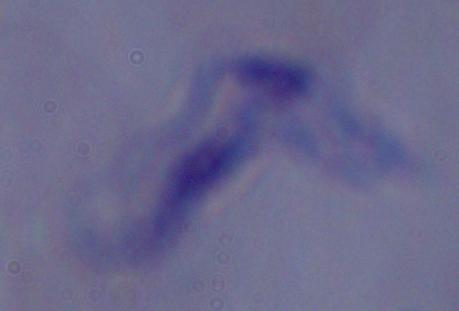
magnification = 1000x
modality = micrograph
identification = trypanosome